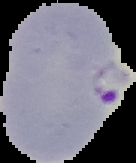
preparation = thin blood smear
malaria status = parasitized
image type = segmented cell region on a black background
image size = 136×163 pixels